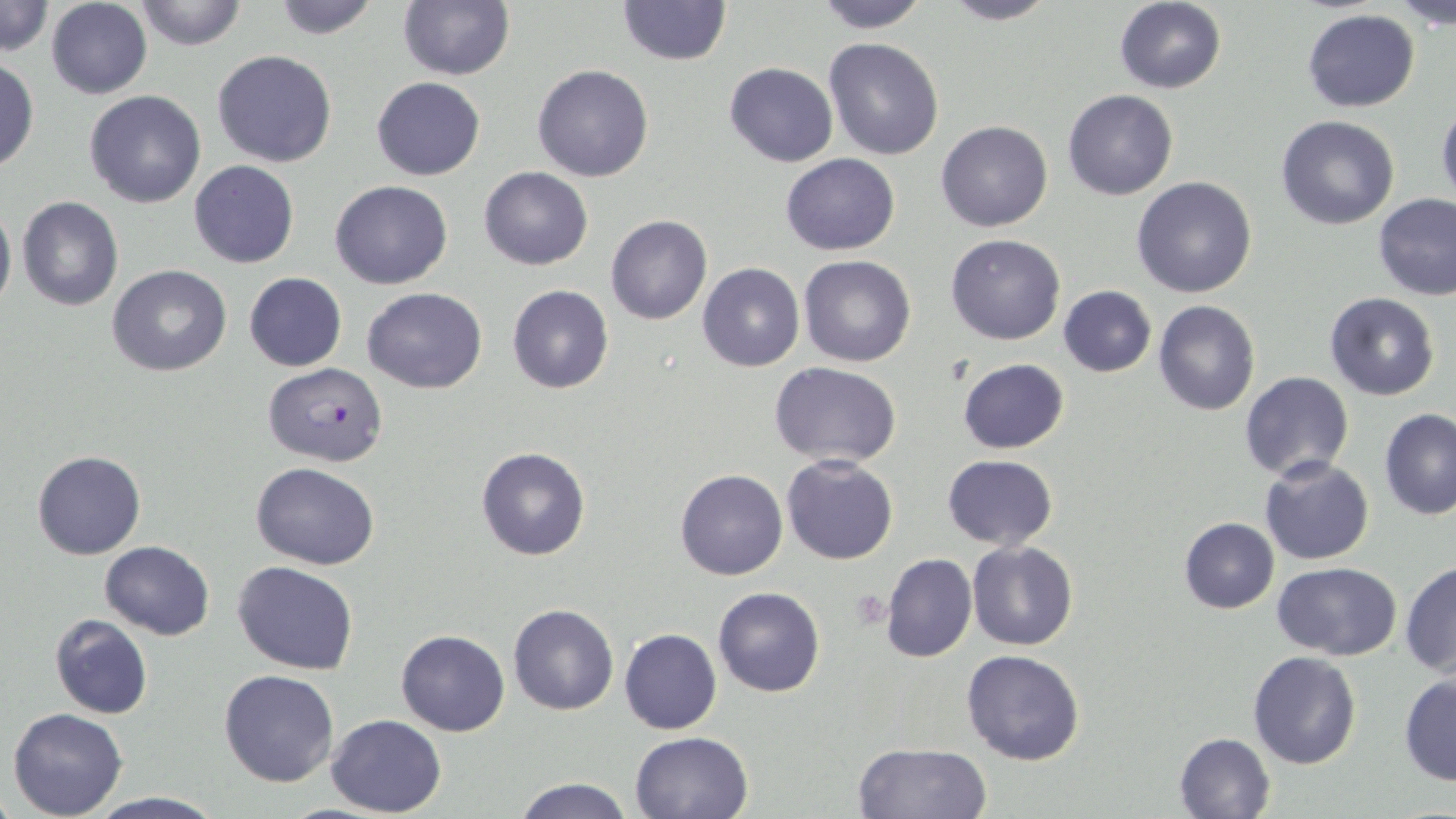

Summary:
  - Coordinate format: approximate bounding boxes as (x1,y1)-(x2,y2) corner pairs in pixels
  - Plasmodium falciparum-infected red blood cell locations: (262,362)-(389,467)
  - Uninfected red blood cell locations: (0,0)-(52,58), (131,0)-(250,52), (269,0)-(386,39), (616,0)-(730,66), (813,0)-(932,32), (935,0)-(1059,25), (1390,1)-(1455,31), (46,2)-(152,99), (396,2)-(515,80), (1114,2)-(1226,94), (1302,9)-(1420,112), (824,37)-(944,159), (212,49)-(339,168), (0,57)-(38,172), (723,62)-(839,167), (533,65)-(655,182), (371,76)-(485,180), (1062,89)-(1178,201), (83,91)-(207,208), (1436,100)-(1456,211), (1276,115)-(1400,230), (936,121)-(1053,232), (780,153)-(901,255), (188,160)-(299,268), (478,167)-(593,270), (1132,177)-(1258,298), (330,179)-(453,290), (1374,194)-(1456,300), (17,197)-(123,311), (0,200)-(16,318), (606,214)-(712,325), (945,233)-(1067,345), (797,255)-(918,368), (698,262)-(804,371), (108,265)-(232,377), (244,272)-(347,372), (507,284)-(613,394), (1057,286)-(1156,376), (361,287)-(487,394), (1324,293)-(1440,401), (1153,301)-(1260,416), (958,358)-(1069,453), (769,361)-(902,467), (1239,370)-(1354,482), (1379,406)-(1456,520), (476,447)-(591,561), (32,450)-(147,560), (942,454)-(1057,550), (781,455)-(899,565), (1261,456)-(1375,565), (250,462)-(379,569), (675,468)-(788,580), (1177,516)-(1280,614), (99,540)-(215,639), (967,540)-(1078,652), (881,553)-(977,664), (233,561)-(360,676), (1271,562)-(1402,660), (1402,562)-(1456,676), (713,586)-(825,697), (507,604)-(619,715), (49,615)-(155,720), (618,628)-(722,735), (396,629)-(510,737), (961,648)-(1087,765), (1247,652)-(1362,770), (218,668)-(340,786), (1399,673)-(1455,785), (6,707)-(128,818), (325,714)-(448,817), (629,730)-(754,819), (1172,732)-(1275,819), (849,741)-(991,818), (512,776)-(636,818), (83,791)-(228,819)
  - Platelet locations: (849,588)-(890,631)
  - Slide-level diagnosis: Plasmodium falciparum
  - Modality: light microscopy
  - Stain: May-Grünwald-Giemsa
  - Magnification: 1000x
  - Image size: 1456×819 pixels
  - Field of view: one of a larger specimen
  - Preparation: thin blood smear